State which parasite is depicted.
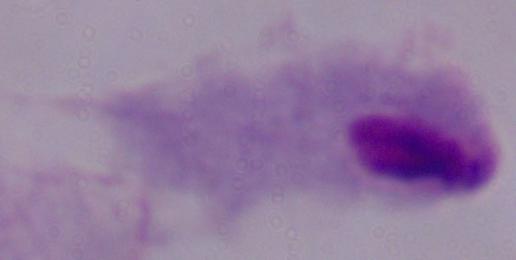

A trichomonad.

Summary:
  - Modality: photomicrograph
  - Magnification: 1000x